Describe the morphology of the erythrocytes.
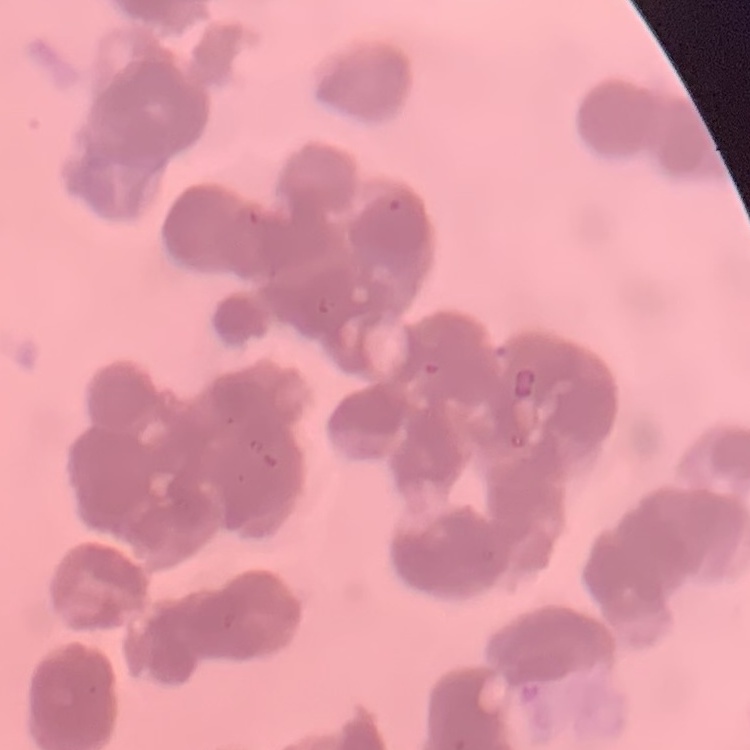

They show rouleaux formation.

Stained with either Field's or Giemsa. Thin blood smear. One tile cut from a larger photomicrograph.